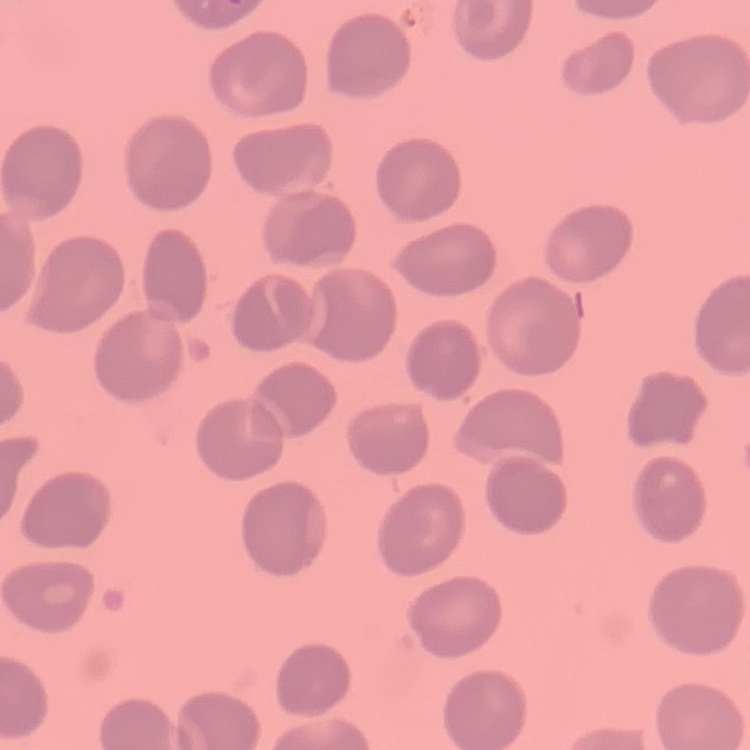

Summary:
  - Red blood cell morphology: no rouleaux formation
  - Stain: Field's or Giemsa
  - Preparation: thin blood film
  - Image type: square crop of a larger photomicrograph